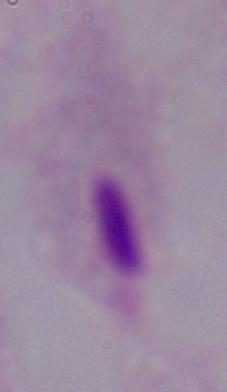 Micrograph. A trichomonad is shown. Captured at 1000x magnification.